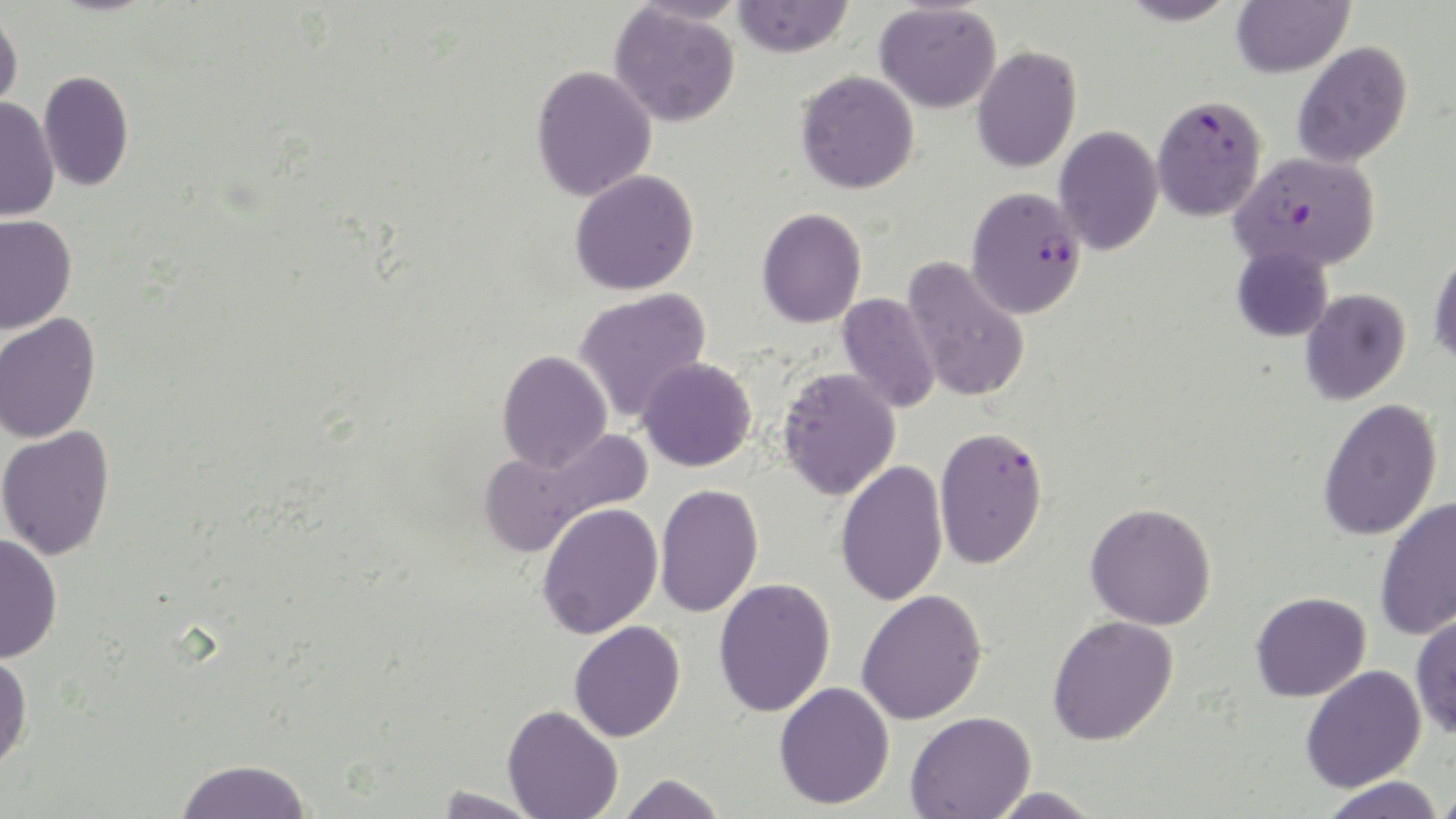

slide-level diagnosis = Plasmodium falciparum
stain = May-Grünwald-Giemsa
modality = optical microscopy
magnification = 1000x
image size = 1456×819 pixels
field of view = one of a larger specimen
uninfected red blood cell locations = approximate bounding boxes as (x1, y1, x2, y2) in pixels: (732, 0, 854, 57), (1119, 0, 1238, 26), (1231, 0, 1354, 78), (874, 2, 1002, 113), (609, 4, 741, 127), (0, 8, 23, 117), (1292, 41, 1413, 168), (972, 45, 1081, 173), (530, 64, 658, 202), (38, 70, 134, 192), (796, 70, 920, 194), (0, 97, 60, 222), (1054, 125, 1163, 255), (570, 169, 700, 295), (756, 208, 867, 328), (0, 214, 77, 334), (1232, 244, 1333, 342), (1428, 246, 1456, 366), (902, 256, 1031, 402), (573, 288, 712, 424), (1299, 288, 1411, 405), (837, 292, 941, 414), (0, 312, 101, 443), (496, 350, 612, 472), (637, 357, 757, 472), (777, 367, 901, 500), (1318, 397, 1443, 541), (0, 426, 115, 561), (479, 427, 653, 557), (835, 459, 948, 607), (655, 484, 764, 619), (1375, 495, 1456, 641), (537, 502, 663, 639), (1085, 502, 1217, 630), (0, 533, 63, 663), (713, 577, 836, 717), (856, 589, 988, 725), (1251, 592, 1371, 702), (1410, 610, 1456, 738), (1047, 615, 1179, 745), (569, 620, 686, 742), (0, 651, 33, 773), (1300, 665, 1426, 793), (774, 681, 895, 810), (503, 704, 623, 819), (905, 711, 1036, 819), (175, 758, 312, 818), (618, 773, 727, 819), (1319, 776, 1447, 819), (1430, 784, 1456, 817), (433, 786, 544, 818), (983, 787, 1104, 818)
Plasmodium falciparum-infected red blood cell locations = approximate bounding boxes as (x1, y1, x2, y2) in pixels: (1151, 94, 1267, 221), (1231, 150, 1380, 271), (966, 186, 1087, 318), (934, 426, 1048, 569)
preparation = thin blood film